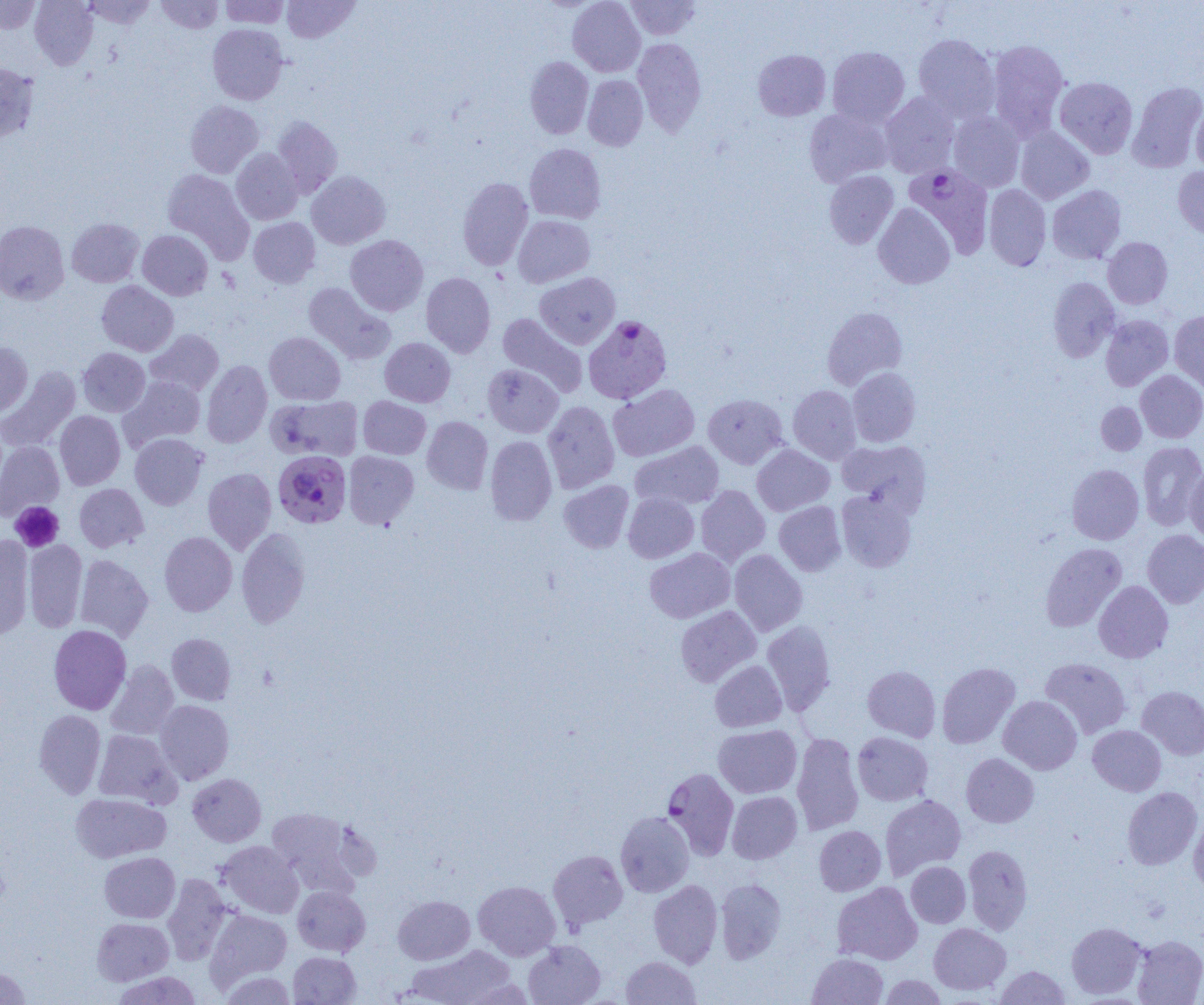
Approximate bounding boxes as (x1,y1)-(x2,y2) corner pairs in pixels. Platelet locations: (10,501)-(64,552). Uninfected red blood cell locations: (0,0)-(41,33), (30,0)-(98,69), (81,0)-(156,29), (156,0)-(224,34), (219,0)-(290,28), (282,0)-(359,43), (567,0)-(645,76), (625,0)-(701,40), (207,24)-(289,105), (913,33)-(999,121), (633,38)-(706,136), (986,39)-(1070,139), (827,46)-(909,126), (752,49)-(830,121), (525,56)-(593,138), (0,62)-(38,142), (583,75)-(649,150), (1054,76)-(1138,159), (1127,81)-(1204,172), (880,92)-(960,178), (1191,99)-(1204,173), (185,100)-(263,178), (804,108)-(893,187), (947,111)-(1025,192), (272,116)-(342,197), (1015,126)-(1094,204), (524,143)-(606,223), (231,149)-(303,224), (1173,166)-(1204,239), (162,169)-(254,262), (824,170)-(898,248), (306,171)-(390,249), (457,177)-(533,270), (984,185)-(1051,270), (1048,185)-(1126,264), (873,203)-(955,289), (513,215)-(595,287), (248,217)-(320,288), (67,218)-(144,287), (0,221)-(69,304), (137,230)-(213,300), (345,235)-(428,316), (1103,237)-(1173,308), (421,272)-(496,358), (535,272)-(620,349), (1048,276)-(1120,362), (97,281)-(178,356), (303,282)-(395,364), (822,306)-(907,390), (1169,311)-(1204,394), (497,313)-(588,397), (1100,315)-(1173,391), (146,329)-(224,396), (264,332)-(345,405), (380,337)-(455,407), (0,342)-(33,417), (77,347)-(150,416), (202,360)-(272,448), (483,364)-(563,437), (1,367)-(80,452), (848,367)-(920,447), (1136,370)-(1204,443), (120,376)-(206,450), (608,383)-(700,461), (788,385)-(861,464), (703,394)-(788,468), (266,395)-(363,461), (358,396)-(430,459), (543,400)-(619,493), (1096,402)-(1146,455), (55,410)-(125,489), (422,416)-(493,494), (130,433)-(208,510), (485,435)-(557,525), (837,440)-(931,513), (0,441)-(64,518), (630,441)-(724,510), (1138,442)-(1204,530), (752,445)-(834,515), (343,451)-(419,529), (1067,464)-(1144,544), (1185,467)-(1204,544), (203,468)-(276,554), (559,480)-(634,553), (75,483)-(148,552), (696,485)-(770,566), (836,489)-(917,572), (623,492)-(699,563), (774,501)-(846,576), (236,528)-(310,628), (1142,529)-(1204,608), (159,531)-(237,616), (0,537)-(34,639), (23,540)-(87,632), (1040,543)-(1127,631), (645,548)-(735,623), (729,549)-(807,636), (75,555)-(154,642), (1093,580)-(1173,663), (675,606)-(761,686), (762,620)-(836,714), (48,625)-(131,714), (167,633)-(236,705), (1040,657)-(1131,738), (106,660)-(179,740), (710,660)-(787,732), (937,662)-(1020,748), (863,665)-(940,742), (1137,686)-(1204,759), (998,695)-(1082,775), (155,700)-(234,784), (34,709)-(106,798), (713,724)-(802,798), (1088,725)-(1166,796), (93,730)-(179,807), (853,731)-(933,805), (792,732)-(863,835), (961,753)-(1039,828), (188,773)-(266,846), (1122,787)-(1202,869), (727,791)-(802,864), (71,793)-(171,862), (880,794)-(966,879), (266,807)-(359,893), (615,811)-(694,897), (1188,814)-(1204,896), (814,825)-(886,896), (216,841)-(303,918), (963,845)-(1033,934), (548,850)-(627,930), (100,852)-(180,923), (906,861)-(970,927), (162,873)-(232,965), (715,878)-(786,963), (649,879)-(722,968), (474,880)-(560,960), (832,882)-(922,965), (292,886)-(370,956), (393,895)-(475,964), (205,909)-(291,986), (92,918)-(174,985), (1067,922)-(1147,999), (929,923)-(1010,995), (1132,935)-(1204,1005), (523,940)-(605,1005), (406,944)-(515,1004), (288,951)-(361,1004), (807,953)-(889,1004), (621,956)-(700,1004), (994,965)-(1070,1004), (0,966)-(31,1005), (112,971)-(203,1005), (221,971)-(296,1004), (879,975)-(946,1004). Plasmodium falciparum-infected red blood cell locations: (905,164)-(994,258), (583,315)-(672,403), (273,450)-(351,528), (662,768)-(739,860). Slide-level diagnosis: Plasmodium falciparum. Light microscopy. Single field of view. Image is 1204×1005 pixels. Captured at 1000x magnification. Thin blood smear.